Locate and identify every blood parasite.
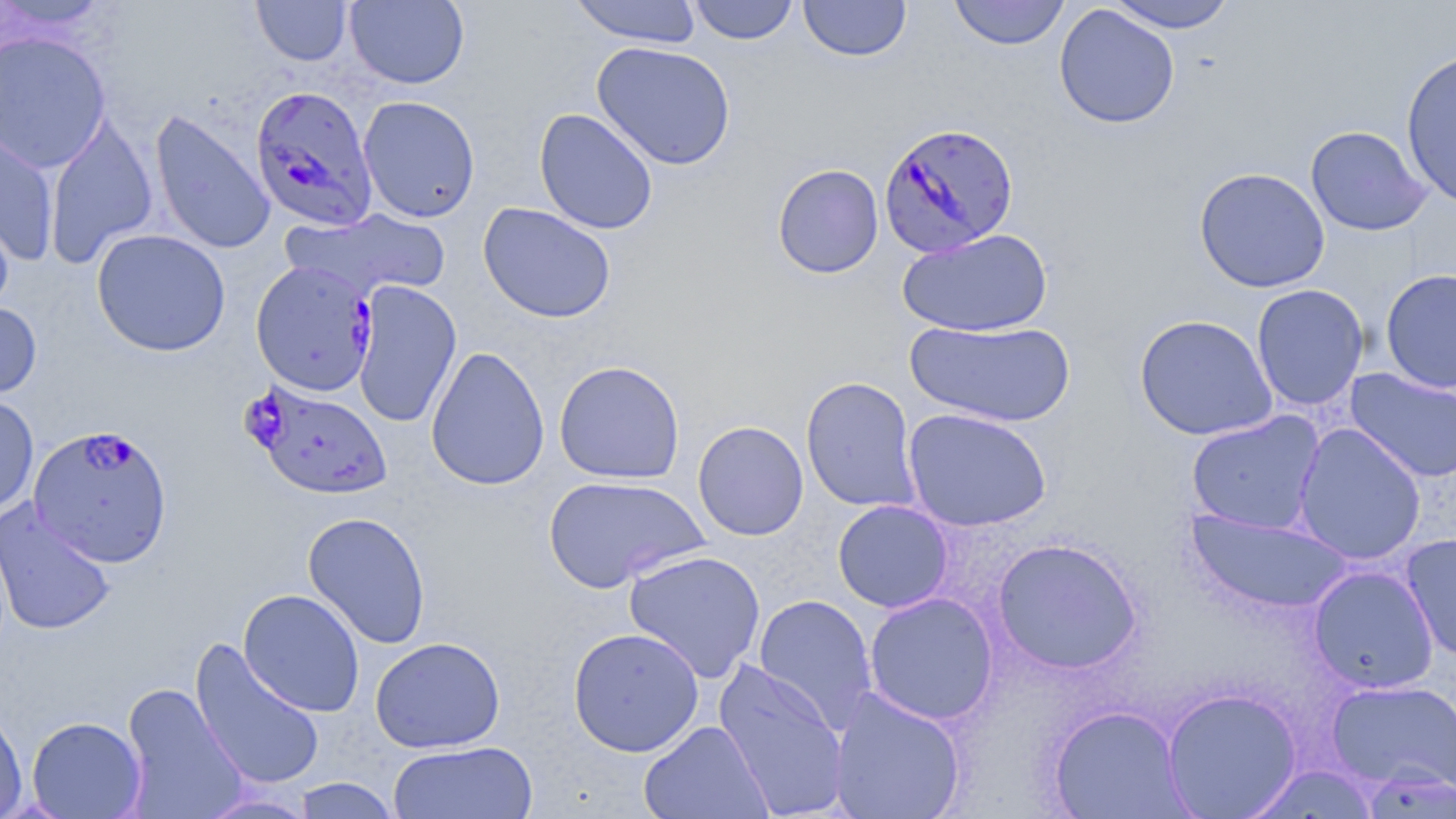

Approximate bounding boxes as (x1, y1, x2, y2) in pixels.
Plasmodium falciparum-infected red blood cells: (250, 85, 378, 230), (879, 122, 1019, 258), (251, 260, 378, 395), (247, 379, 393, 499), (28, 425, 174, 569).
No Plasmodium ovale, Plasmodium malariae, Plasmodium vivax, Babesia divergens, or Trypanosoma brucei observed.

Summary:
  - Uninfected red blood cell locations: (0, 0, 115, 35), (345, 0, 469, 89), (568, 0, 703, 47), (688, 0, 799, 45), (798, 0, 911, 62), (948, 0, 1070, 50), (1106, 0, 1236, 33), (251, 1, 353, 65), (1054, 4, 1180, 129), (0, 31, 111, 172), (591, 41, 736, 171), (1401, 48, 1456, 210), (358, 95, 480, 223), (149, 108, 276, 254), (534, 108, 659, 235), (43, 112, 159, 268), (0, 119, 59, 265), (1305, 124, 1432, 236), (772, 163, 884, 278), (1194, 167, 1330, 293), (0, 199, 16, 315), (478, 202, 616, 323), (282, 209, 451, 302), (91, 228, 231, 357), (896, 228, 1053, 337), (1380, 268, 1456, 394), (351, 281, 462, 428), (1250, 284, 1369, 411), (0, 299, 42, 403), (1134, 314, 1278, 441), (905, 318, 1076, 427), (425, 345, 550, 492), (553, 360, 685, 484), (1345, 368, 1456, 483), (800, 376, 921, 513), (0, 393, 39, 516), (902, 407, 1052, 532), (1186, 411, 1325, 535), (693, 420, 809, 541), (1293, 423, 1427, 565), (542, 474, 709, 593), (1, 499, 116, 637), (832, 499, 954, 613), (1186, 508, 1353, 614), (302, 511, 432, 649), (1400, 533, 1456, 662), (992, 537, 1144, 675), (623, 549, 766, 683), (1307, 565, 1439, 695), (238, 588, 366, 717), (863, 592, 999, 725), (753, 594, 878, 734), (567, 626, 705, 757), (370, 636, 505, 753), (189, 637, 326, 792), (713, 658, 850, 818), (1325, 677, 1456, 794), (120, 683, 248, 818), (828, 687, 967, 819), (1161, 688, 1302, 818), (0, 704, 28, 819), (1049, 705, 1190, 818), (26, 716, 147, 818), (639, 720, 774, 819), (387, 740, 538, 819), (291, 777, 401, 818), (194, 790, 321, 818)
  - Slide-level diagnosis: Plasmodium falciparum
  - Magnification: 1000x
  - Modality: optical microscopy
  - Image size: 1456×819 pixels
  - Field of view: single
  - Preparation: thin blood film
  - Stain: May-Grünwald-Giemsa